Comment on the morphology of the erythrocytes.
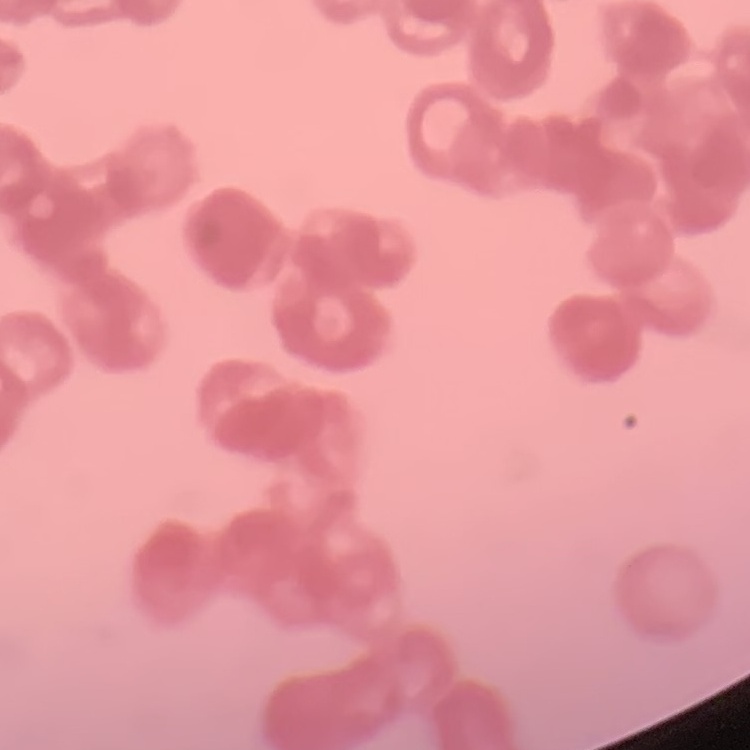

Rouleaux formation.

Summary:
  - Image type: one tile cut from a larger photomicrograph
  - Preparation: thin blood smear
  - Stain: Field's or Giemsa